Report the malaria status of this cell.
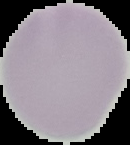

Uninfected.

Summary:
  - Image type: segmented cell region on a black background
  - Image size: 130×145 pixels
  - Preparation: thin blood smear